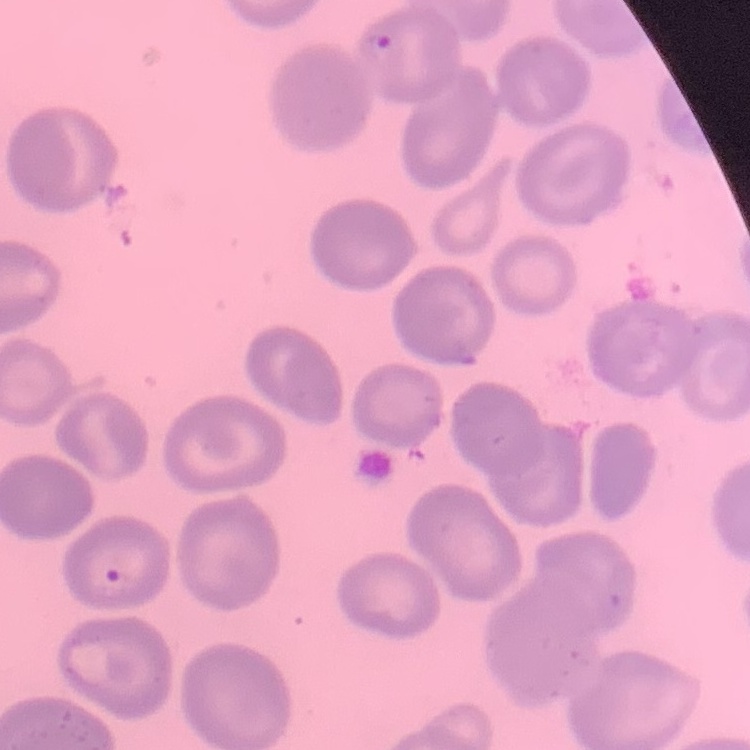 The erythrocytes exhibit no rouleaux formation. Field's or Giemsa stain. One tile cut from a larger photomicrograph. Thin peripheral smear.